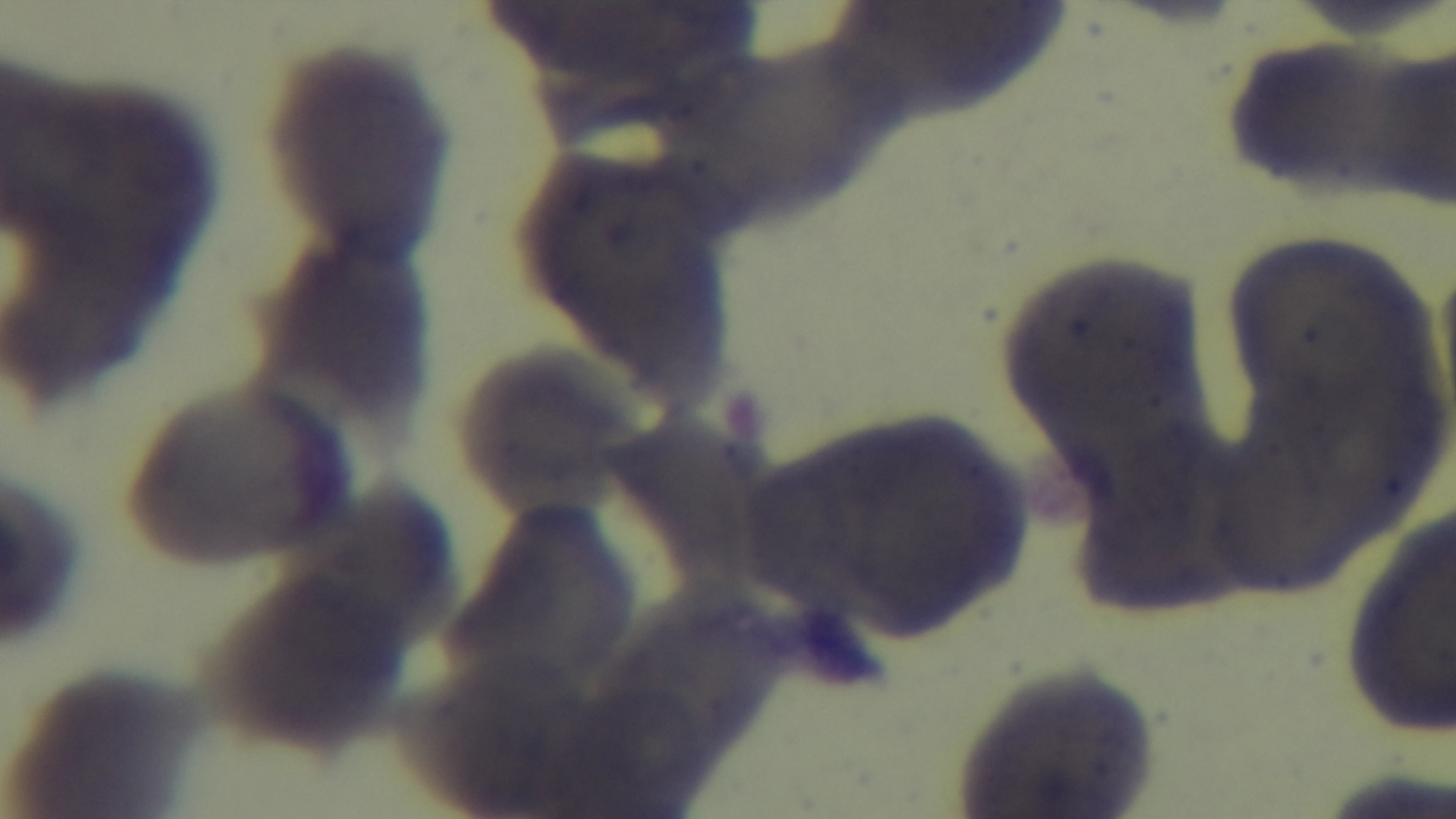

Preparation: thin blood film. Captured with a mounted 4K digital camera. One field from the slide. Giemsa stain. Photomicrograph. 100x oil-immersion objective. Malaria status: uninfected.